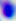
Summary:
  - Modality: micrograph
  - Identification: Toxoplasma gondii
  - Magnification: 400x